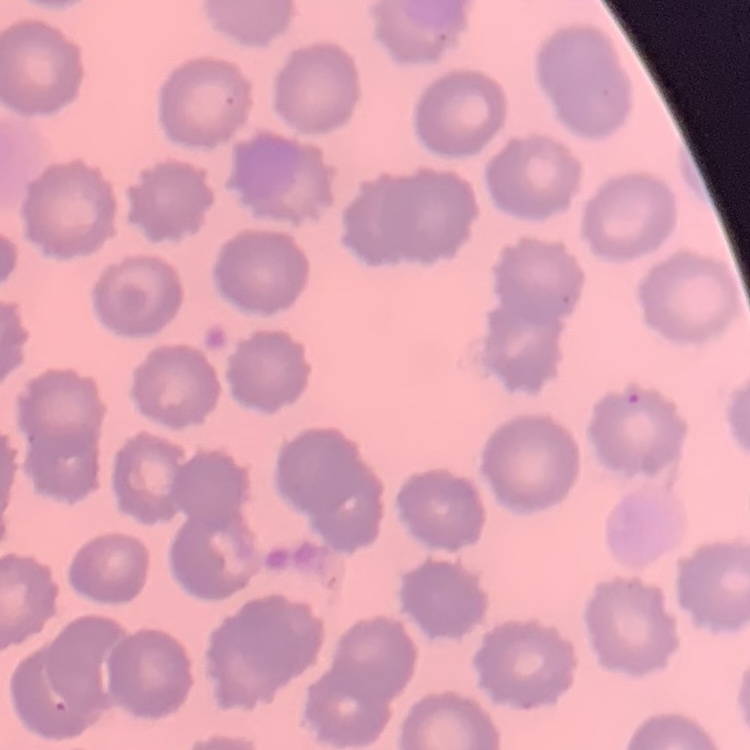
red blood cell morphology = no rouleaux formation
stain = Field's or Giemsa
image type = square crop of a larger photomicrograph
preparation = thin peripheral smear